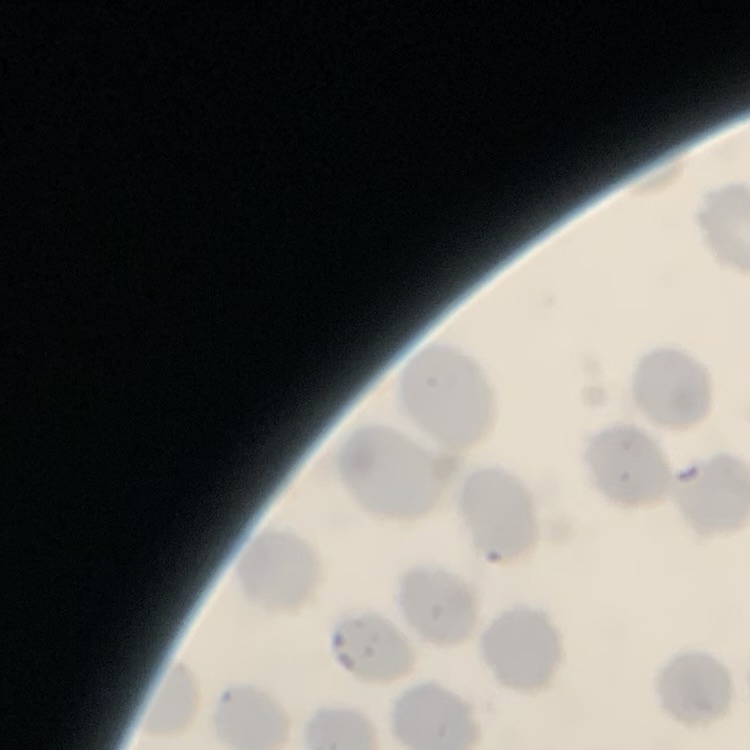
The erythrocytes show no rouleaux formation. Stained with either Field's or Giemsa. Thin blood smear. One tile cut from a larger photomicrograph.